Look for parasitized red blood cells.
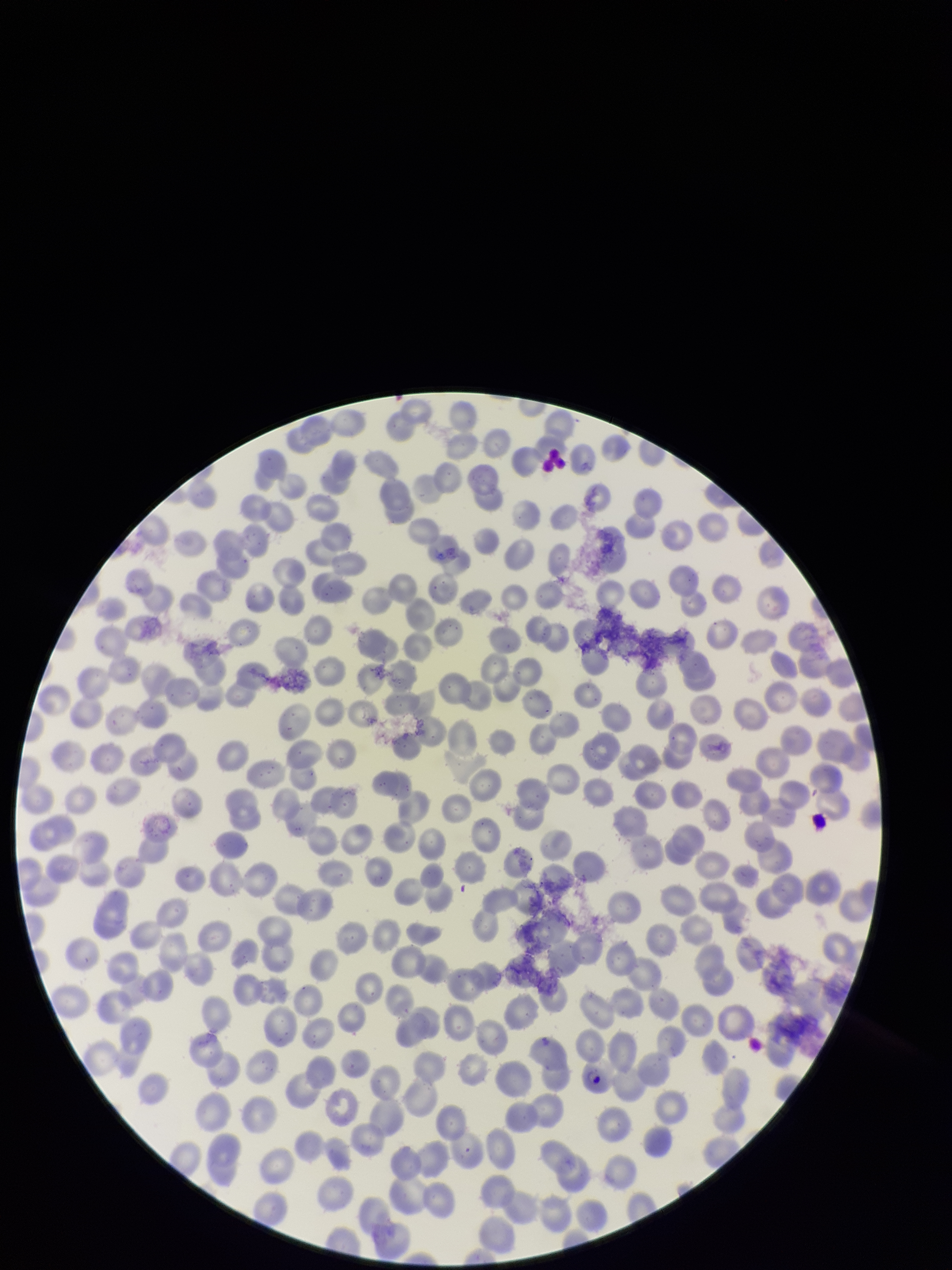
Detected.

Stained with Giemsa. Parasitized red blood cell count: 1. One field from this slide. Preparation: thin smear. Red blood cell count: 316. Image is 952×1270 pixels. Species reported for this patient: Plasmodium falciparum. Smartphone photograph taken through the eyepiece of a microscope. Patient malaria status: infected.